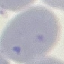
result = no malaria parasites detected
preparation = thin smear
capture = smartphone camera at the microscope eyepiece
image type = automatically extracted cell patch, resized to 64 × 64 pixels
stain = Giemsa